Name the parasite shown.
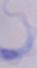
A trypanosome.

1000x magnification. Photomicrograph.